Identify the parasite.
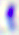
Toxoplasma gondii.

Micrograph. Captured at 400x magnification.